Assess this cell for malaria.
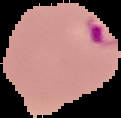

It is parasitized.

Image is 121×118 pixels. From a thin blood smear. Segmented cell region on a black background.